Locate every Plasmodium parasite by life-cycle stage, and every leukocyte.
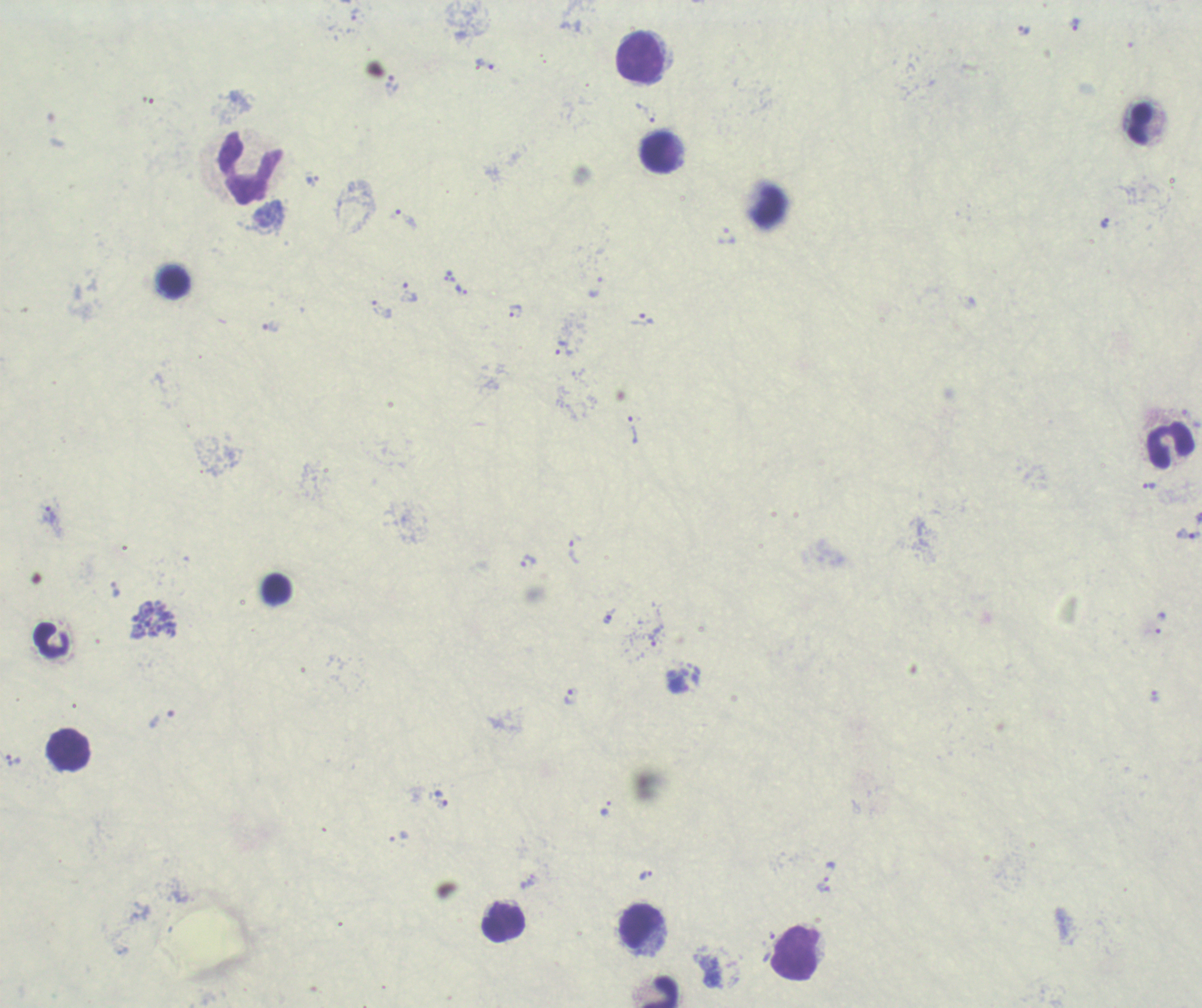
Approximate centers as [x, y] in pixels.
Trophozoites: [355, 14], [1074, 25], [1024, 31], [484, 63], [392, 84], [645, 112], [311, 180], [407, 219], [1105, 223], [727, 236], [595, 287], [461, 289], [409, 293], [382, 310], [515, 310], [641, 319], [270, 327], [563, 348], [632, 430], [1149, 486], [48, 514], [1188, 534], [574, 552], [528, 561], [115, 589], [609, 614], [1160, 623], [654, 637], [571, 695], [1154, 696], [440, 798], [605, 809], [830, 871], [646, 874], [823, 888].
Schizonts: [152, 620].
No gametocyte forms observed.
Leukocytes: [641, 59], [1140, 124], [660, 151], [251, 168], [174, 281], [1170, 447], [275, 588], [51, 640], [68, 749], [503, 923], [642, 928], [796, 953], [659, 991].

Summary:
  - Preparation: thick blood smear
  - Image size: 1202×1008 pixels
  - Stain: Romanowsky
  - Context: previously used in a real diagnosis
  - Magnification: 100x
  - Field of view: single
  - Background quality: unsatisfactory